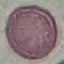

result = no malaria parasites detected
image type = automatically extracted cell patch, resized to 64 × 64 pixels
capture = smartphone through the microscope eyepiece
stain = Giemsa
preparation = thin blood smear